Report the malaria status of this cell.
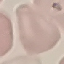
It is uninfected.

Summary:
  - Preparation: thin blood film
  - Stain: Giemsa
  - Capture: smartphone through the microscope eyepiece
  - Image type: cell patch, automatically extracted from a larger field of view and resized to 64 × 64 pixels